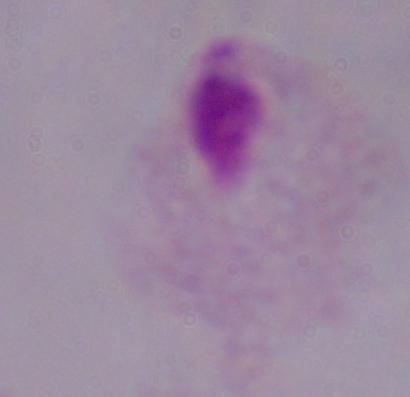

Summary:
  - Identification: trichomonad
  - Modality: micrograph
  - Magnification: 1000x